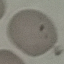

Summary:
  - Malaria status: uninfected
  - Capture: smartphone camera at the microscope eyepiece
  - Image type: automatically extracted cell patch, resized to 64 × 64 pixels
  - Stain: Giemsa
  - Preparation: thin smear